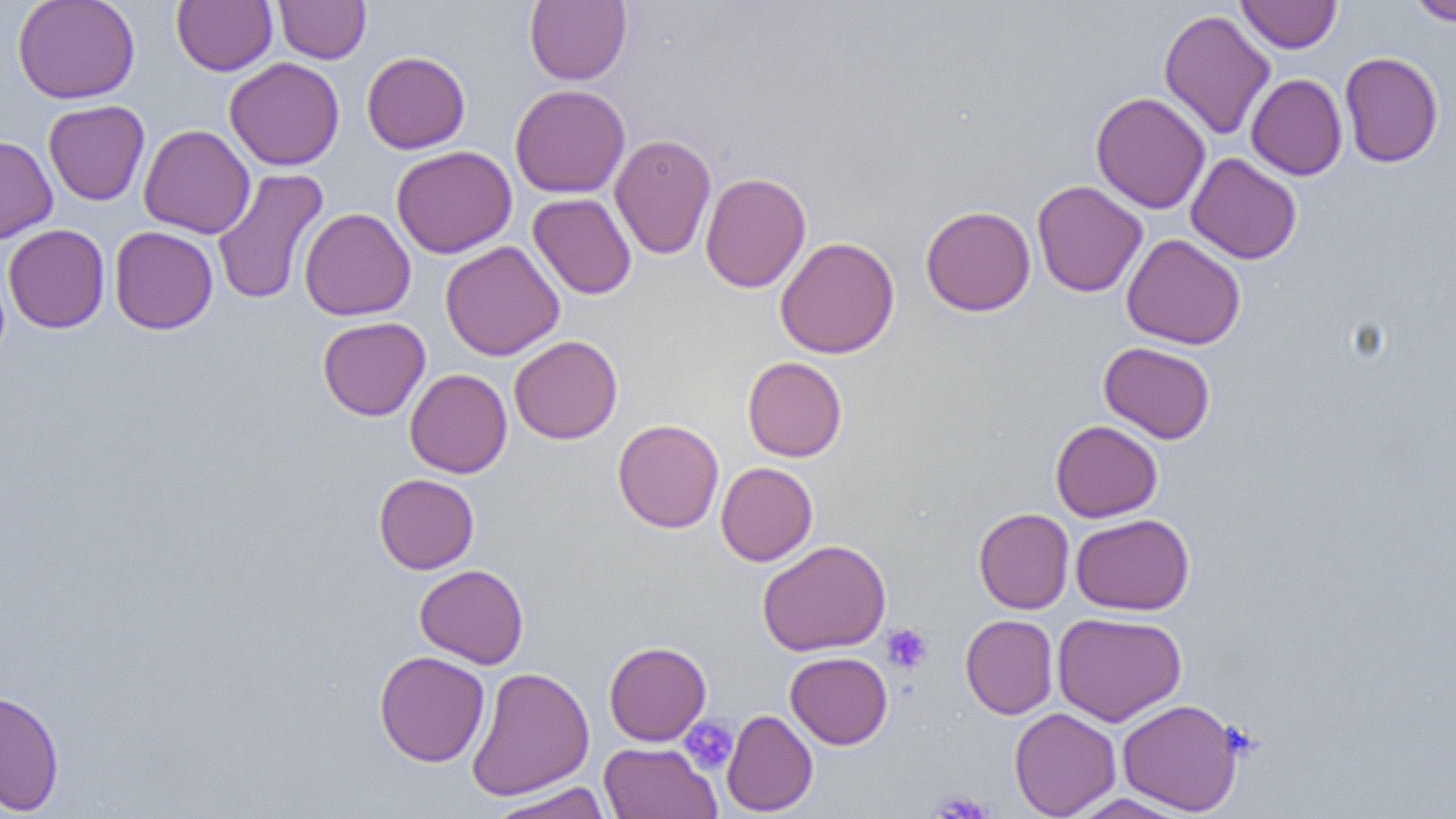

Summary:
  - Coordinate format: approximate bounding boxes as (x1,y1)-(x2,y2) corner pairs in pixels
  - Uninfected red blood cell locations: (12,0)-(140,104), (172,0)-(277,76), (274,0)-(370,64), (524,0)-(632,85), (1236,0)-(1341,53), (1406,0)-(1455,25), (1159,9)-(1275,140), (362,51)-(470,154), (1340,51)-(1444,167), (225,57)-(345,170), (1246,74)-(1347,180), (510,84)-(630,198), (1091,92)-(1210,214), (43,100)-(150,206), (139,123)-(255,239), (609,133)-(717,260), (0,135)-(58,244), (391,145)-(517,259), (1186,152)-(1302,264), (211,168)-(329,306), (699,172)-(811,293), (1032,180)-(1148,297), (528,192)-(637,299), (921,205)-(1036,316), (299,207)-(415,321), (3,224)-(110,333), (109,226)-(218,334), (1122,232)-(1246,350), (774,237)-(900,359), (440,241)-(564,361), (317,316)-(430,421), (509,335)-(623,445), (1099,341)-(1216,443), (742,357)-(847,462), (405,369)-(512,478), (612,418)-(724,534), (1050,420)-(1162,522), (716,462)-(818,567), (374,473)-(479,574), (973,508)-(1074,613), (1070,513)-(1195,615), (757,539)-(891,656), (414,564)-(529,668), (1052,611)-(1187,727), (960,614)-(1058,719), (604,641)-(711,746), (374,650)-(490,767), (785,651)-(892,749), (466,666)-(594,800), (0,688)-(65,815), (1117,699)-(1243,815), (1009,708)-(1121,818), (721,709)-(818,816), (599,741)-(721,819), (487,781)-(612,818), (1067,794)-(1194,818)
  - Platelet locations: (881,622)-(933,674), (679,716)-(738,774), (930,789)-(993,818)
  - Slide-level diagnosis: no evidence of blood parasites
  - Image size: 1456×819 pixels
  - Preparation: thin blood smear
  - Magnification: 1000x
  - Modality: optical microscopy
  - Field of view: single